Outline every leukocyte.
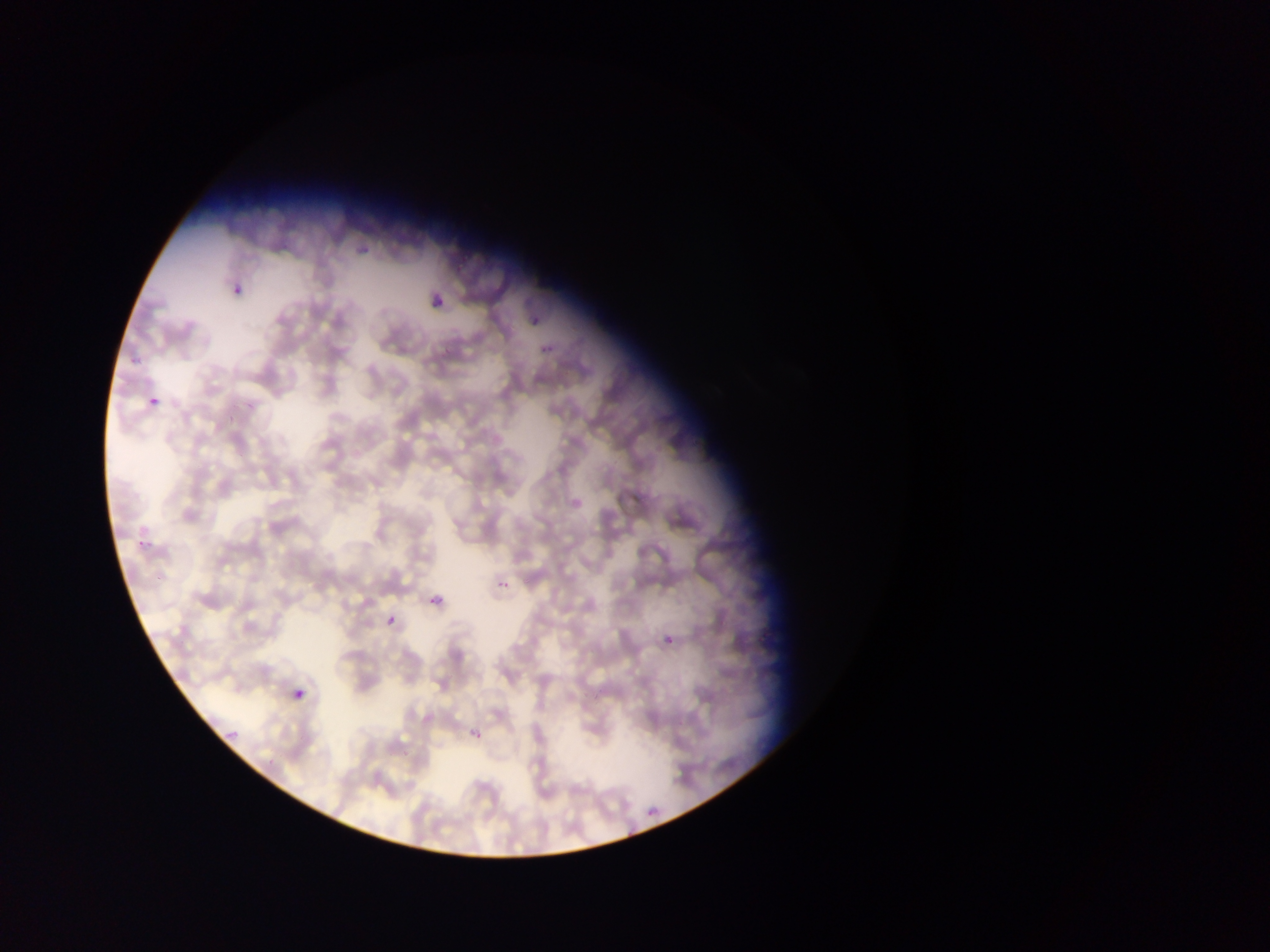
No leukocytes observed.

Approximate bounding boxes as (left, top, right, bottom) in pixels. Malaria parasite locations: (353, 237, 379, 256), (229, 277, 251, 294), (427, 290, 444, 309), (528, 309, 545, 325), (130, 351, 142, 368), (148, 392, 166, 406), (136, 524, 160, 551), (495, 575, 514, 598), (425, 589, 452, 617), (382, 607, 401, 626), (662, 632, 679, 650), (289, 682, 313, 709), (221, 725, 243, 738), (466, 725, 486, 746), (644, 798, 666, 822). Thin blood film. Image is 1270×952 pixels. Sample from Ghana. Single field of view. Photographed through a microscope with a mobile-phone camera.